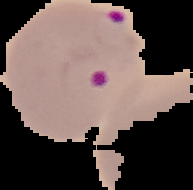 From a thin blood film. Segmented cell region on a black background. Result: Plasmodium parasites detected. Image is 193×190 pixels.